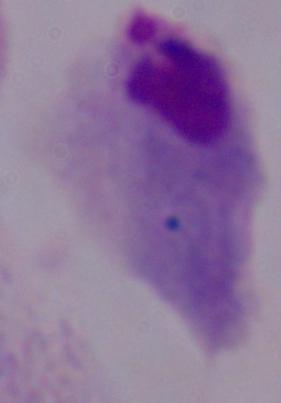

1000x magnification. A trichomonad is seen. Photomicrograph.